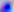
Summary:
  - Magnification: 400x
  - Identification: Toxoplasma gondii
  - Modality: photomicrograph